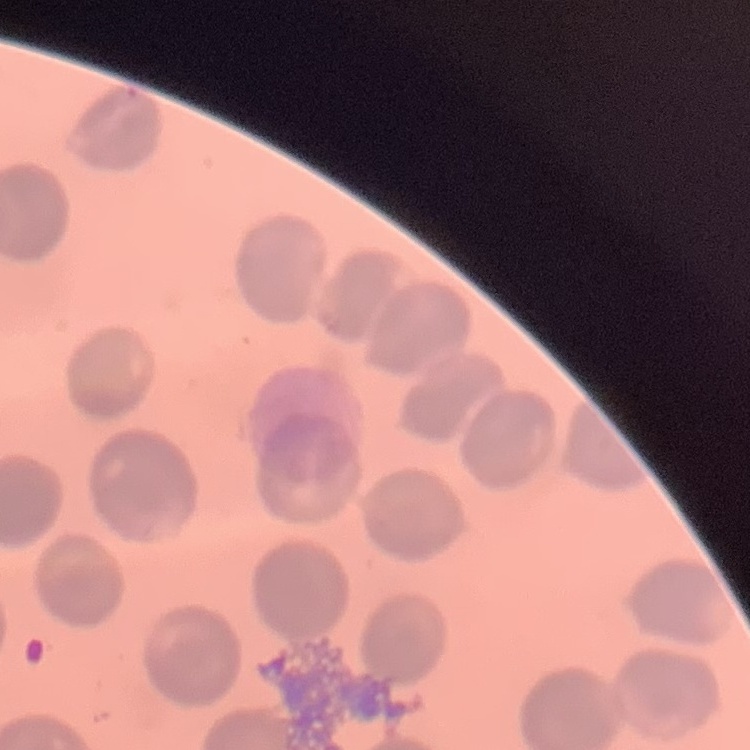

red blood cell morphology = no rouleaux formation
image type = square crop of a larger photomicrograph
preparation = thin blood film
stain = Field's or Giemsa